Name the blood parasite species.
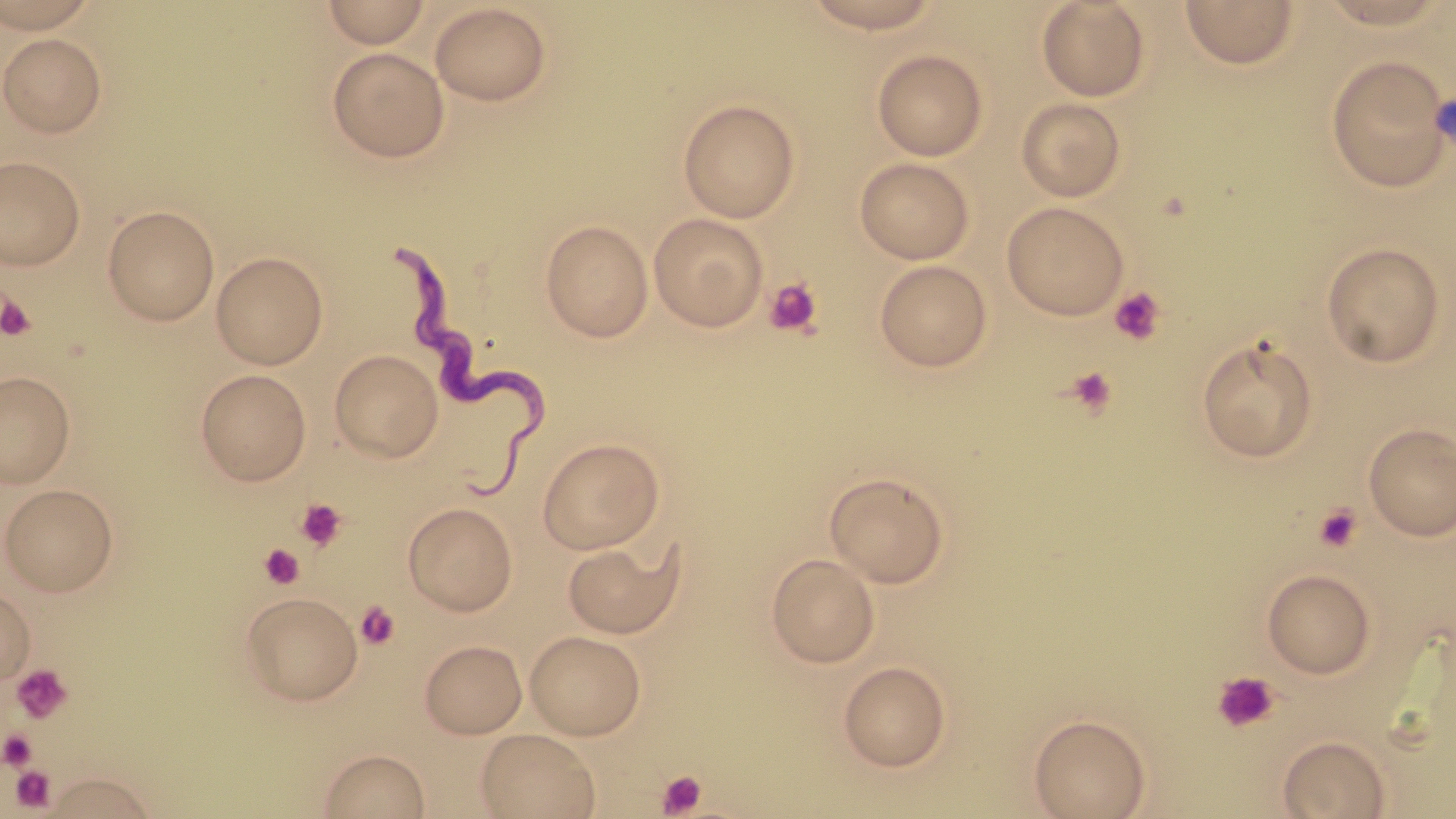

Trypanosoma brucei.

Approximate bounding boxes as (x1,y1)-(x2,y2) corner pairs in pixels. Trypanosoma brucei locations: (395,250)-(550,506). Uninfected red blood cell locations: (0,0)-(102,32), (322,0)-(430,48), (799,0)-(947,34), (1036,0)-(1151,102), (1312,0)-(1455,30), (1180,1)-(1300,69), (429,3)-(551,106), (0,33)-(107,137), (327,47)-(450,162), (871,49)-(989,161), (1325,56)-(1452,192), (1016,97)-(1126,202), (678,98)-(800,223), (0,156)-(86,270), (854,157)-(975,264), (1001,201)-(1128,320), (102,205)-(220,325), (648,213)-(769,332), (540,219)-(653,343), (1320,241)-(1446,368), (211,251)-(328,369), (874,259)-(993,372), (1196,336)-(1319,463), (330,349)-(443,462), (195,369)-(312,485), (0,371)-(76,488), (1363,423)-(1456,541), (537,437)-(665,554), (824,472)-(950,588), (1,483)-(119,596), (403,502)-(518,616), (562,537)-(686,640), (766,553)-(880,668), (1261,568)-(1376,679), (0,586)-(36,685), (240,591)-(363,705), (525,630)-(646,740), (419,639)-(527,738), (838,660)-(951,772), (1029,714)-(1150,819), (476,728)-(601,818), (1278,734)-(1391,818), (317,748)-(430,818), (39,771)-(163,817). Platelet locations: (763,276)-(823,338), (1109,287)-(1165,345), (1,294)-(37,342), (1064,366)-(1118,418), (294,498)-(347,551), (1313,503)-(1364,553), (259,544)-(305,589), (356,601)-(400,650), (10,663)-(73,723), (1212,670)-(1279,733), (0,729)-(38,770), (10,765)-(56,812), (656,770)-(707,817). Light microscopy. Single field of view. May-Grünwald-Giemsa stain. Captured at 1000x magnification. Image is 1456×819 pixels. Thin blood film.